Locate every blood parasite and identify its species.
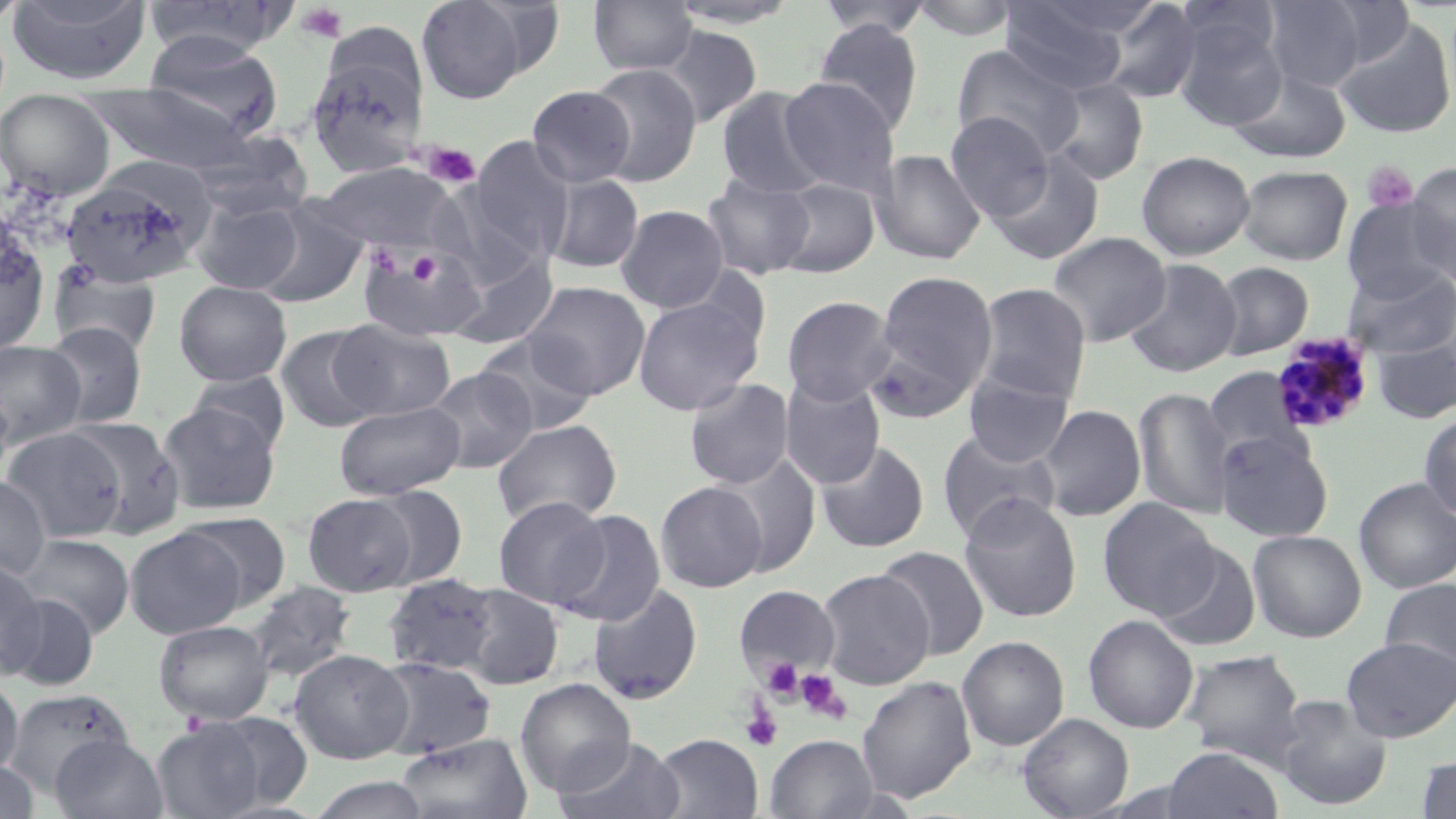

Approximate bounding boxes as [x1, y1, x2, y2] in pixels.
Plasmodium malariae-infected red blood cells: [1270, 334, 1375, 435].
No Plasmodium falciparum, Plasmodium ovale, Plasmodium vivax, Babesia divergens, or Trypanosoma brucei observed.

Uninfected red blood cell locations: [0, 0, 28, 31], [8, 0, 153, 85], [415, 0, 535, 104], [588, 0, 698, 76], [666, 0, 799, 29], [814, 0, 935, 39], [908, 0, 1021, 41], [1261, 0, 1382, 91], [143, 1, 291, 59], [999, 1, 1132, 96], [1095, 1, 1204, 104], [1172, 18, 1288, 131], [1333, 18, 1456, 141], [813, 19, 924, 134], [657, 25, 762, 128], [143, 30, 284, 140], [952, 44, 1085, 162], [307, 54, 428, 178], [587, 63, 702, 186], [1228, 66, 1351, 164], [1044, 76, 1149, 186], [777, 77, 902, 196], [87, 83, 255, 174], [526, 85, 635, 188], [715, 87, 830, 200], [0, 89, 115, 200], [945, 112, 1054, 221], [185, 130, 313, 221], [468, 137, 575, 263], [871, 149, 986, 265], [986, 151, 1105, 264], [1137, 151, 1255, 260], [315, 162, 462, 255], [1405, 162, 1456, 282], [1236, 164, 1352, 265], [61, 169, 212, 288], [701, 173, 815, 281], [545, 174, 644, 274], [771, 177, 880, 278], [428, 183, 542, 291], [252, 196, 370, 308], [1342, 196, 1455, 305], [192, 198, 305, 294], [615, 205, 729, 313], [0, 231, 51, 358], [1046, 232, 1171, 347], [358, 243, 485, 342], [446, 250, 558, 351], [1124, 258, 1241, 378], [1212, 261, 1314, 360], [48, 262, 163, 356], [1342, 266, 1456, 360], [871, 270, 999, 410], [174, 280, 292, 386], [523, 281, 650, 399], [973, 282, 1091, 405], [633, 293, 764, 416], [782, 295, 897, 406], [330, 319, 456, 420], [40, 321, 150, 429], [275, 325, 385, 434], [476, 333, 599, 436], [1371, 338, 1456, 423], [0, 340, 85, 447], [424, 366, 537, 474], [1203, 366, 1310, 467], [187, 370, 291, 453], [963, 371, 1074, 467], [780, 375, 886, 489], [684, 379, 795, 490], [0, 387, 14, 482], [1133, 387, 1235, 520], [334, 400, 464, 499], [158, 402, 281, 515], [1035, 404, 1146, 522], [1419, 410, 1456, 522], [69, 416, 187, 537], [492, 418, 622, 528], [1, 426, 126, 542], [937, 428, 1062, 541], [1213, 431, 1334, 543], [815, 440, 930, 553], [716, 453, 822, 577], [0, 475, 51, 580], [1353, 477, 1456, 593], [656, 481, 767, 593], [366, 485, 467, 589], [958, 492, 1083, 622], [303, 493, 417, 596], [493, 496, 609, 609], [1097, 497, 1220, 620], [552, 509, 667, 627], [180, 512, 291, 612], [124, 527, 246, 638], [1247, 529, 1367, 642], [14, 534, 134, 638], [1153, 543, 1261, 652], [874, 545, 990, 660], [0, 559, 44, 678], [816, 568, 935, 690], [383, 573, 500, 676], [1380, 577, 1456, 679], [244, 580, 357, 684], [587, 583, 704, 704], [458, 584, 564, 690], [733, 584, 840, 682], [3, 593, 100, 691], [1083, 615, 1198, 734], [154, 619, 274, 725], [958, 635, 1069, 751], [1341, 636, 1456, 742], [289, 648, 413, 764], [1180, 649, 1306, 766], [371, 656, 497, 761], [857, 675, 976, 804], [0, 677, 23, 776], [515, 678, 636, 799], [5, 687, 133, 795], [1273, 697, 1392, 811], [1017, 713, 1134, 818], [151, 717, 272, 819], [396, 732, 531, 818], [650, 733, 763, 819], [766, 734, 878, 818], [50, 735, 168, 819], [554, 736, 686, 819], [1162, 746, 1283, 819], [1413, 754, 1456, 818], [0, 759, 39, 818], [306, 774, 430, 818]. Platelet locations: [296, 4, 347, 43], [423, 142, 481, 188], [1363, 161, 1418, 212], [761, 658, 803, 700], [794, 669, 850, 722], [741, 705, 783, 751]. Slide-level diagnosis: Plasmodium malariae. Single field of view. Thin blood film. May-Grünwald-Giemsa stain. Captured at 1000x magnification. Image is 1456×819 pixels. Optical microscopy.